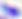
modality = photomicrograph
identification = Toxoplasma gondii
magnification = 400x